Name the cell type shown.
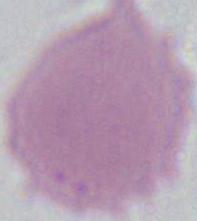
This is an erythrocyte.

modality: photomicrograph
magnification: 1000x